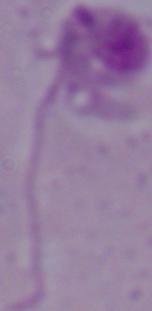
A Leishmania parasite is shown. Captured at 1000x magnification. Photomicrograph.